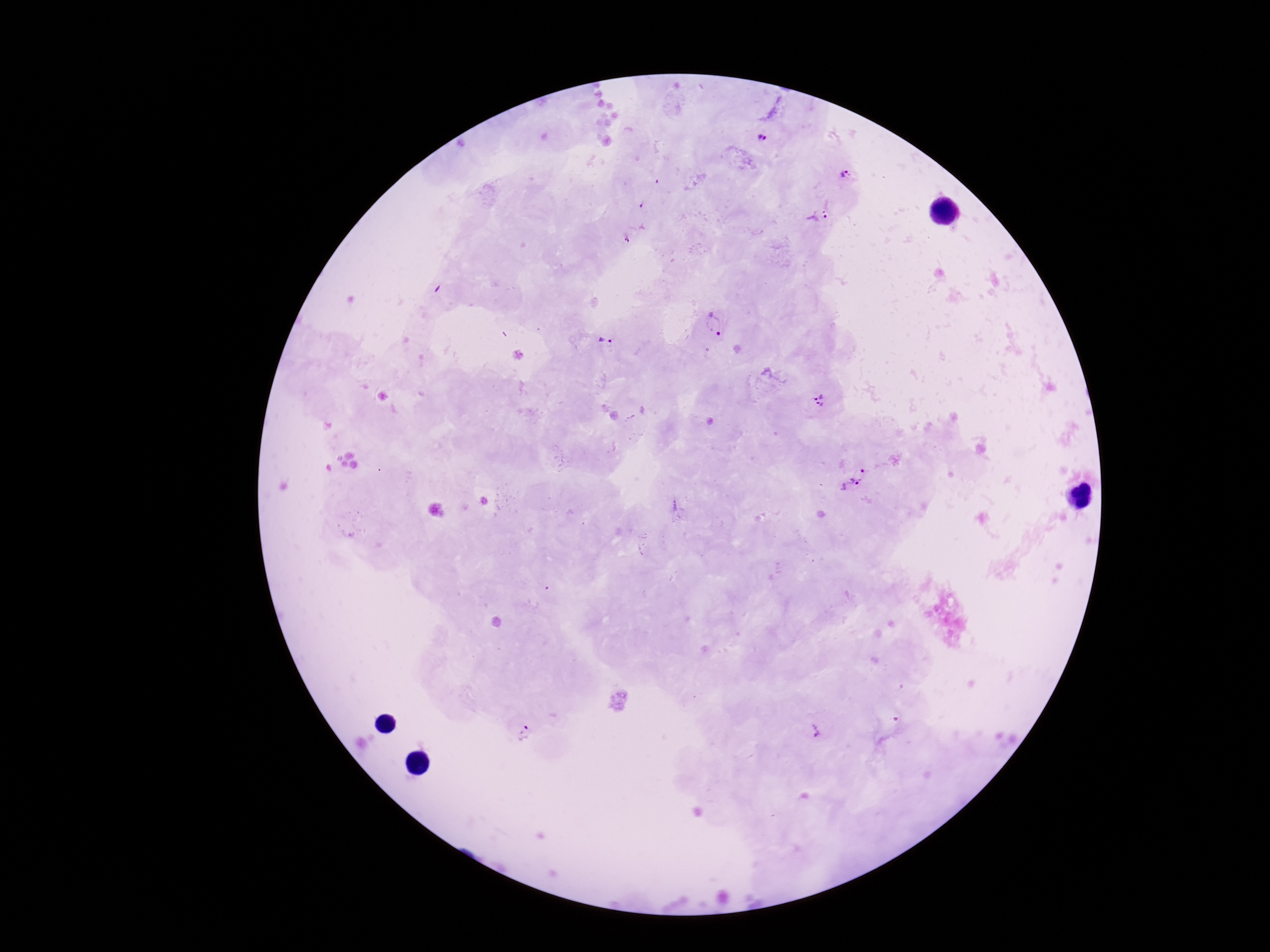 Approximate centers as [x, y] in pixels. Plasmodium parasite locations: [763, 139], [845, 175], [818, 216], [625, 236], [714, 325], [606, 341], [818, 401], [860, 474], [848, 485], [813, 731], [523, 732]. Giemsa stain. Image is 1270×952 pixels. Photographed through the microscope eyepiece with a smartphone camera. 100x magnification. Thick blood film. One field from this slide. Patient malaria status: positive.